Classify this cell by malaria status.
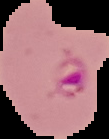
Parasitized.

Segmented cell region on a black background. From a thin blood film. Image is 109×139 pixels.